Classify this cell by malaria status.
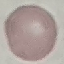

It is uninfected.

Photographed with a smartphone camera at the microscope eyepiece. Thin smear of blood. Cell patch, automatically extracted from a larger field of view and resized to 64 × 64 pixels. Giemsa stain.